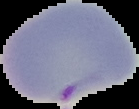 The area outside the segmented cell region is set to black. Image is 139×109 pixels. Malaria status: parasitized. From a thin blood smear.